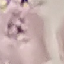 Malaria status: uninfected. Photographed with a smartphone camera at the microscope eyepiece. Giemsa stain. Automatically extracted cell patch, resized to 64 × 64 pixels. Thin blood film.